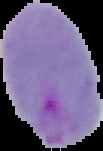
The area outside the segmented cell region is set to black. From a thin blood smear. Image is 103×151 pixels. Result: Plasmodium parasites detected.